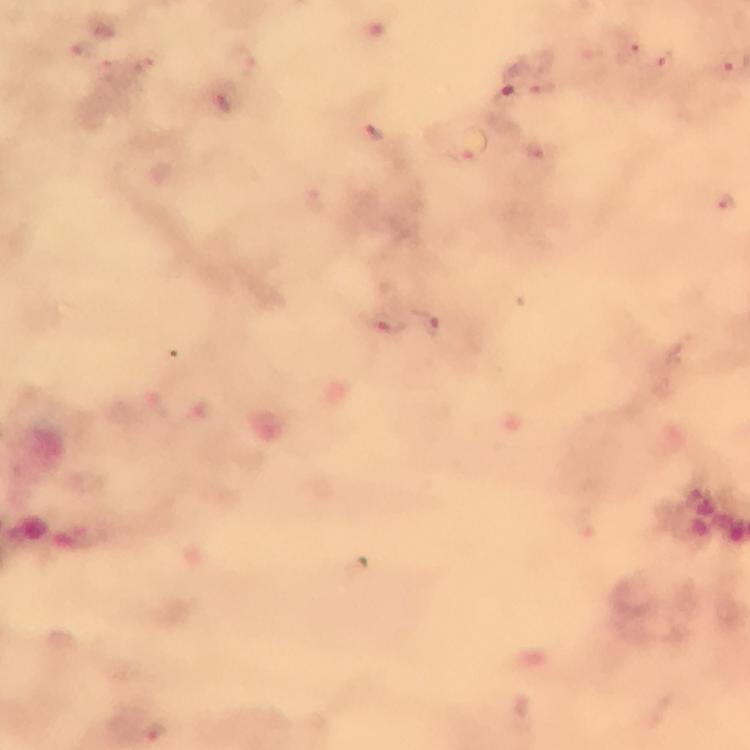

cropped from = a single field of view
malaria parasite locations = approximate object centers, in pixels from the top-left corner: (x=628, y=55), (x=668, y=63), (x=542, y=85), (x=221, y=100), (x=374, y=132), (x=470, y=146), (x=727, y=204), (x=390, y=322), (x=433, y=327)
magnification = 100x
image size = 750×750 pixels
stain = Giemsa
immersion oil = used
capture = smartphone camera through the microscope
context = from a diagnostic examination for malaria
preparation = thick blood film